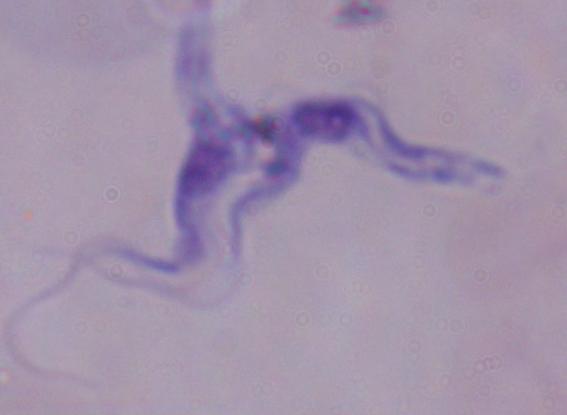
Captured at 1000x magnification. A trypanosome is seen. Micrograph.